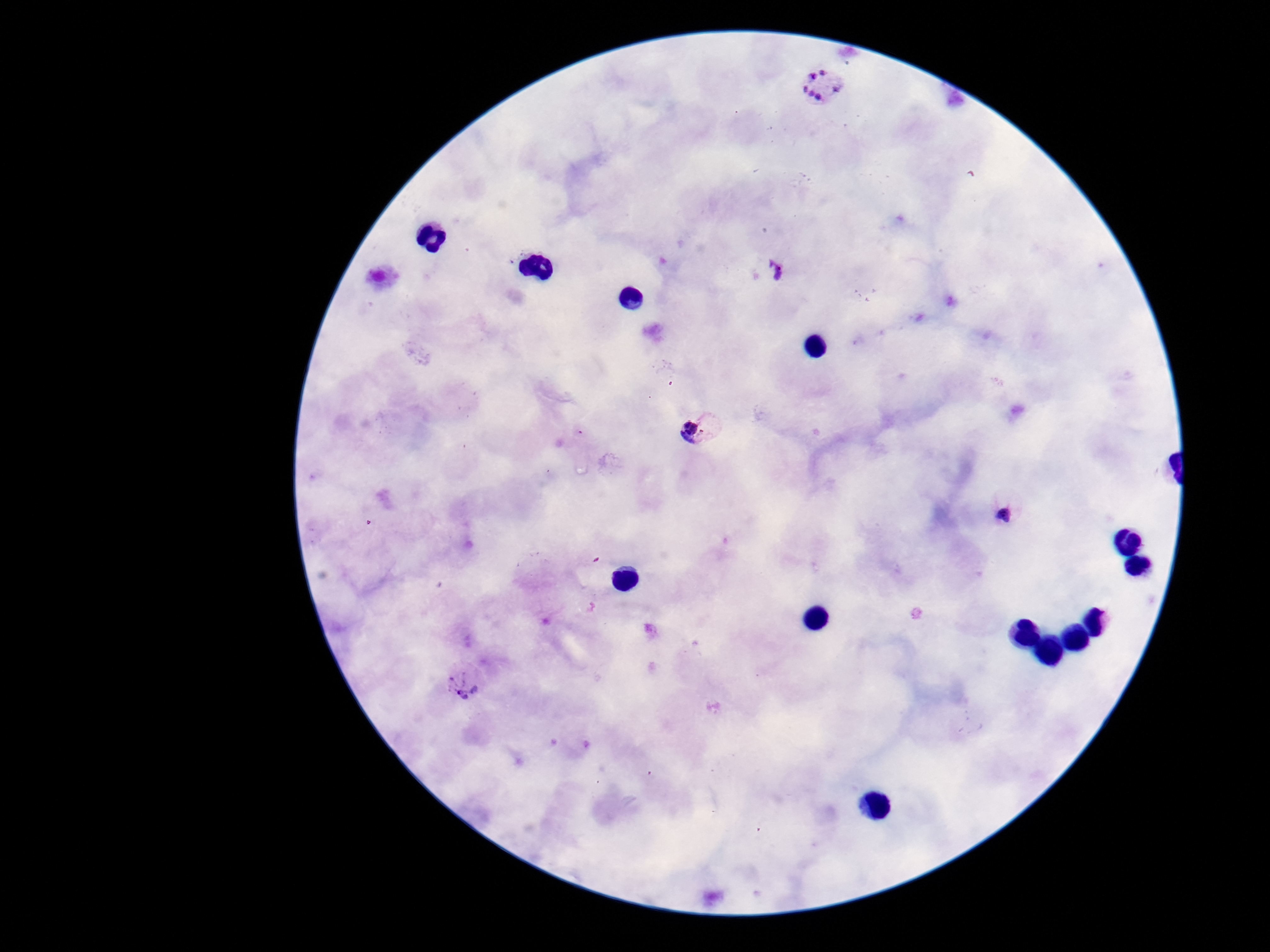
stain = Giemsa
image size = 1270×952 pixels
patient malaria status = positive
Plasmodium parasite locations = approximate centers as (x, y) in pixels: (823, 85), (774, 269), (700, 425), (1002, 509), (465, 676)
preparation = thick blood film
magnification = 100x
capture = smartphone camera through the microscope eyepiece
field of view = one from this slide